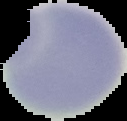

Summary:
  - Image size: 127×121 pixels
  - Result: no malaria parasites seen
  - Preparation: thin blood smear
  - Image type: cell region segmented out of the field of view; surrounding area masked to black